Comment on the morphology of the red blood cells.
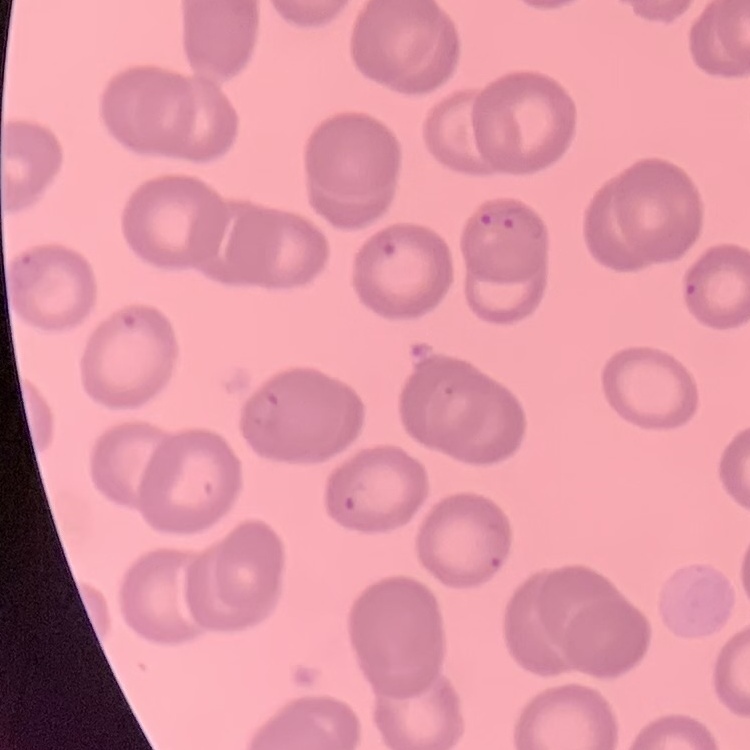

They show no rouleaux formation.

{
  "image_type": "one tile cut from a larger photomicrograph",
  "preparation": "thin blood film",
  "stain": "Field's or Giemsa"
}